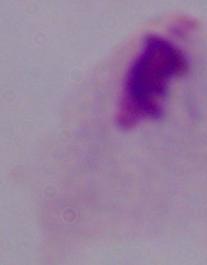

Summary:
  - Magnification: 1000x
  - Identification: trichomonad
  - Modality: photomicrograph